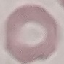

Result: negative for malaria parasites. Thin smear of blood. Photographed with a smartphone camera at the microscope eyepiece. Automatically extracted cell patch, resized to 64 × 64 pixels. Giemsa-stained preparation.